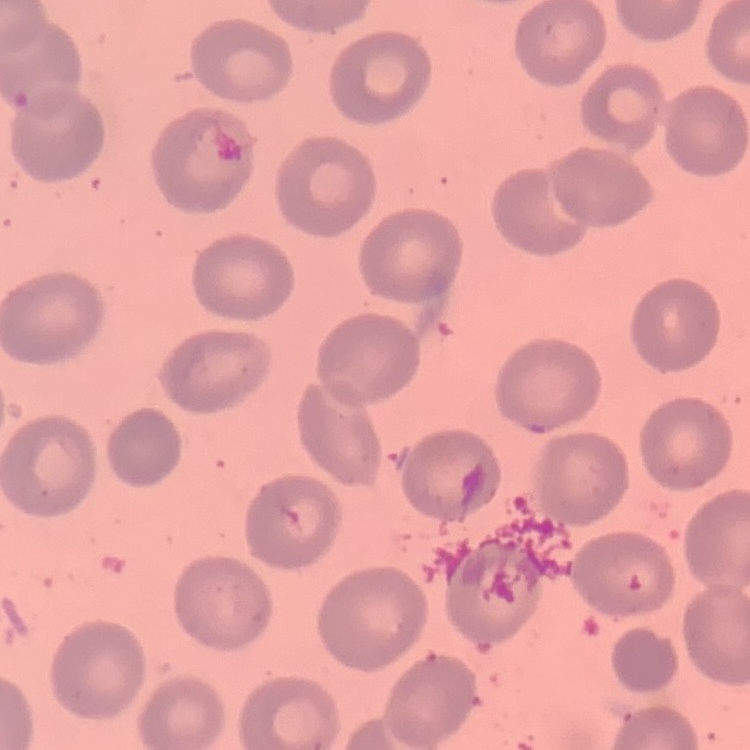
Summary:
  - Erythrocyte morphology: no rouleaux formation
  - Preparation: thin blood film
  - Image type: square crop of a larger photomicrograph
  - Stain: Field's or Giemsa